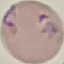
Summary:
  - Malaria status: parasitized
  - Preparation: thin smear
  - Image type: automatically extracted cell patch, resized to 64 × 64 pixels
  - Stain: Giemsa
  - Capture: smartphone camera at the microscope eyepiece